Assess for Plasmodium parasites.
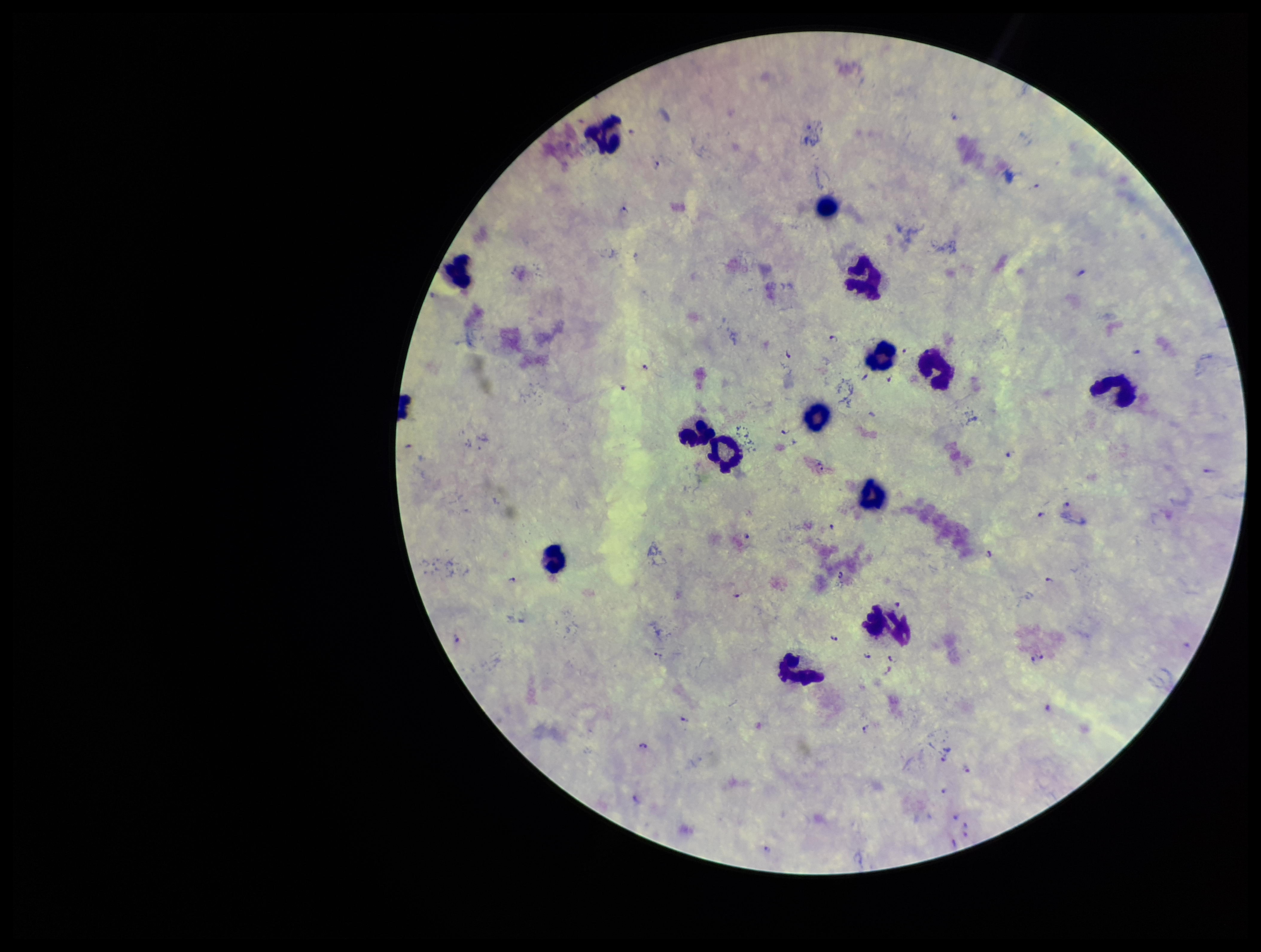
Detected.

capture = smartphone photograph through the microscope eyepiece
stain = Giemsa
parasite count = 41
image size = 1261×952 pixels
species reported for this patient = Plasmodium falciparum
leukocyte count = 14
field of view = single
preparation = thick
patient malaria status = infected